Give the preparation type.
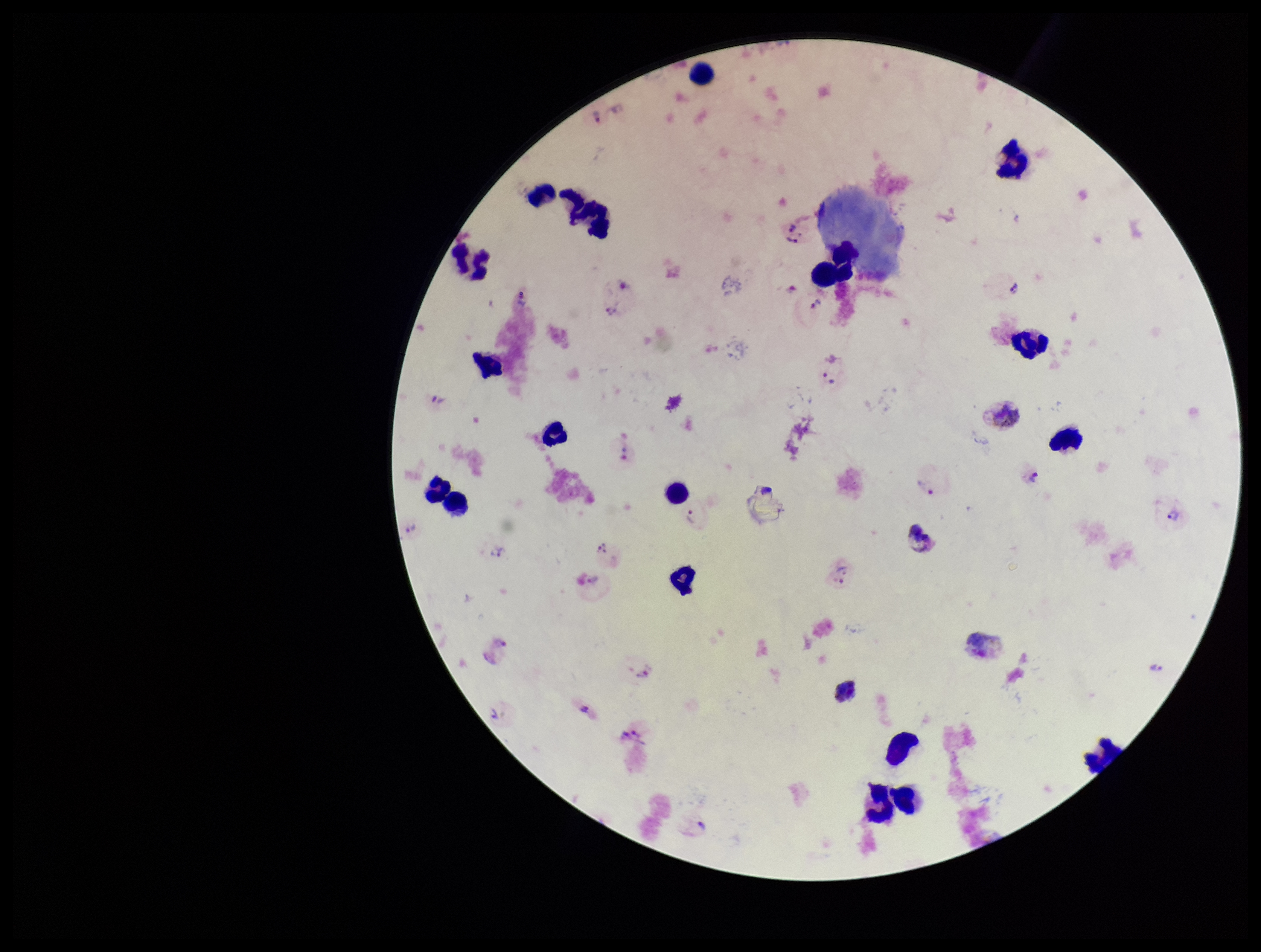
It is a thick blood smear.

stain = Giemsa
parasite count = 31
patient malaria status = infected
field of view = single
Plasmodium parasites = seen
image size = 1261×952 pixels
species reported for this patient = Plasmodium vivax
capture = smartphone photograph through the microscope eyepiece
leukocyte count = 21